Report the malaria status of this cell.
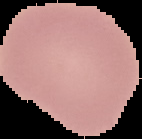

It is uninfected.

Summary:
  - Image type: segmented cell region on a black background
  - Image size: 142×139 pixels
  - Preparation: thin blood smear